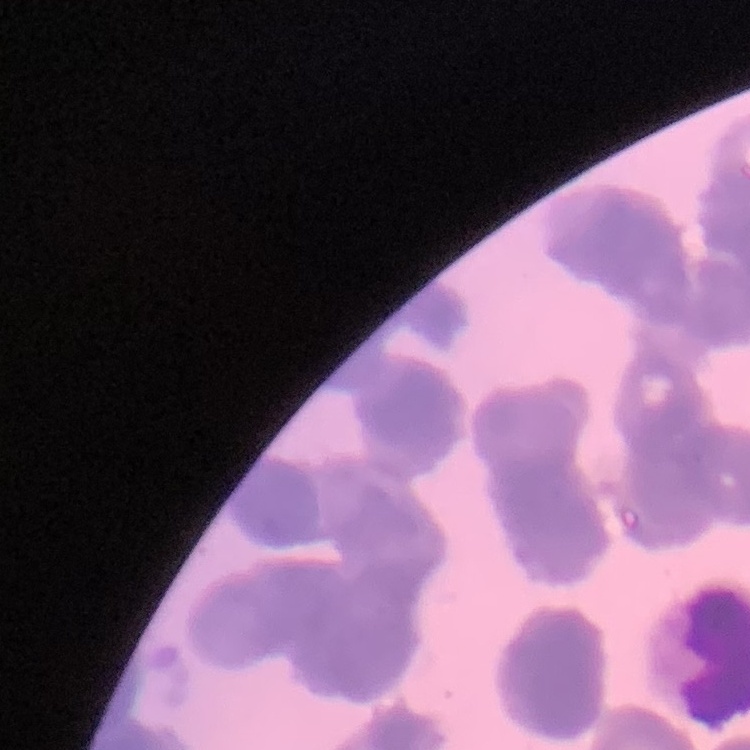
erythrocyte morphology = rouleaux formation
preparation = thin blood film
stain = Field's or Giemsa
image type = square crop of a larger photomicrograph